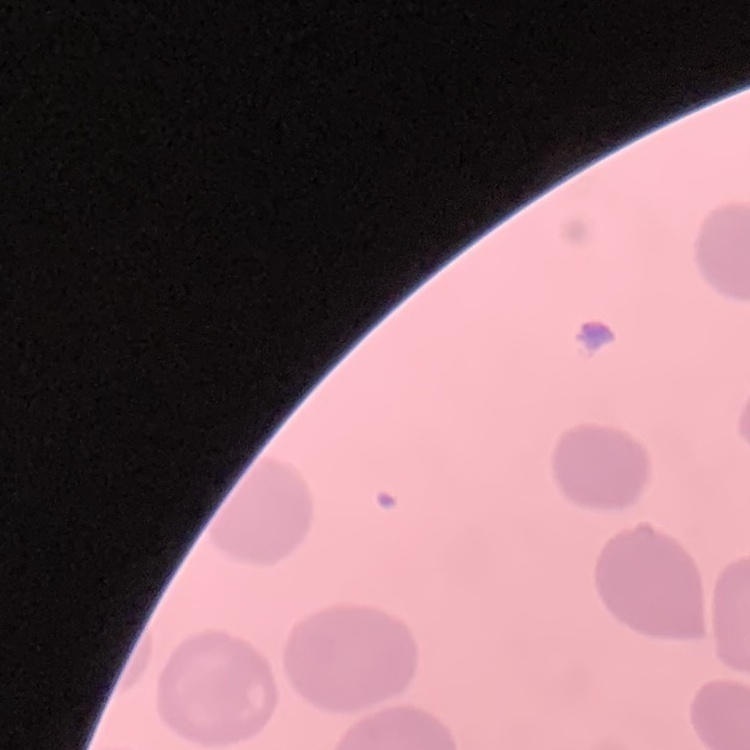

Summary:
  - Red blood cell morphology: no rouleaux formation
  - Image type: square crop of a larger photomicrograph
  - Stain: Field's or Giemsa
  - Preparation: thin blood smear